Give a bounding box for every leukocyte visible.
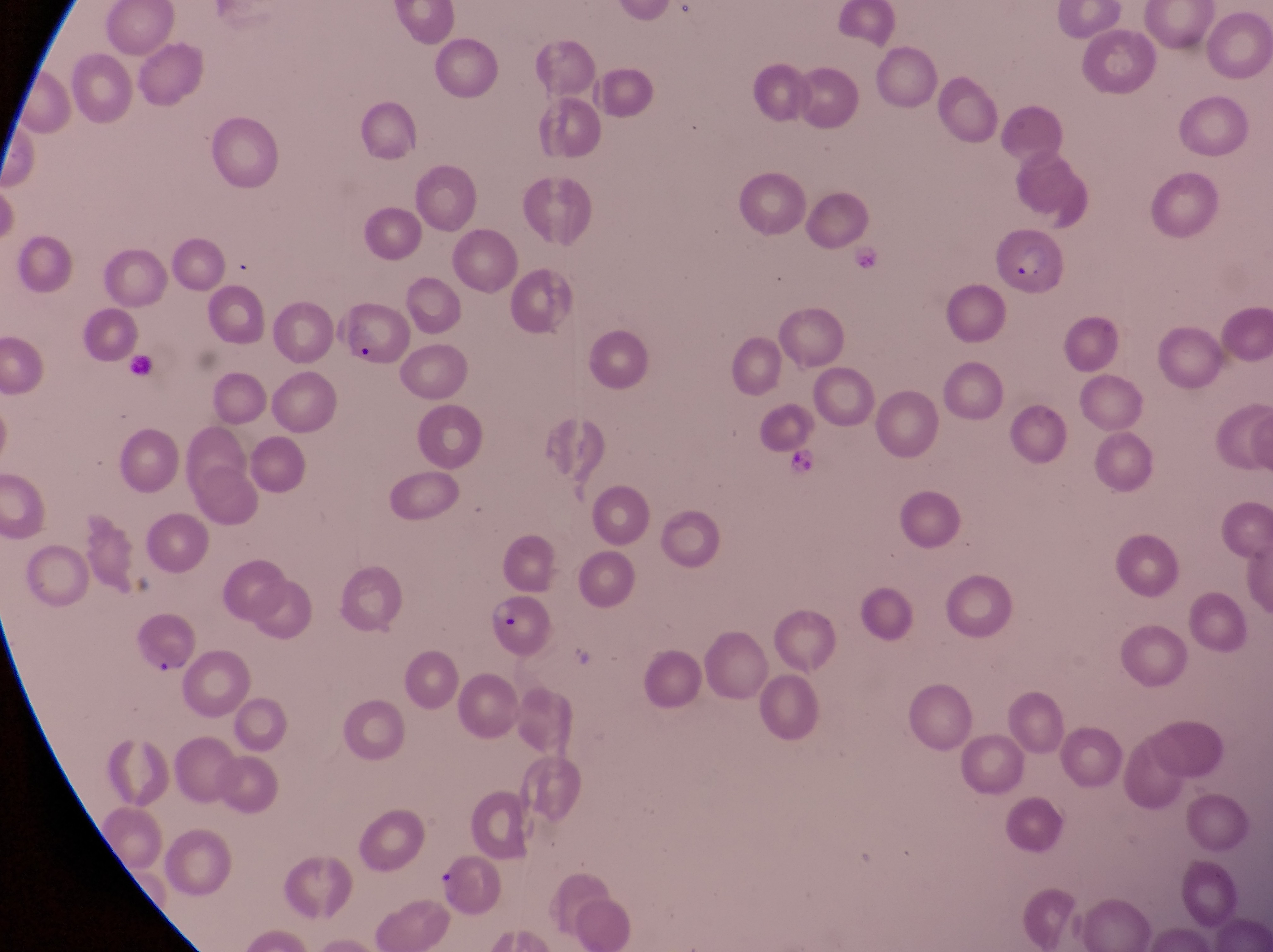

No leukocytes observed.

Approximate bounding boxes as (left, top, right, bottom) in pixels. Parasitised red blood cell locations: (986, 230, 1068, 297), (330, 305, 415, 372), (482, 594, 554, 664), (135, 619, 205, 679). One field of view. Image is 1273×952 pixels. Photographed through the eyepiece of an Olympus CX-23 microscope with a smartphone camera. Thin blood smear. At a magnification of 1000x. Sample from Uganda.